Outline each blood parasite and name the species.
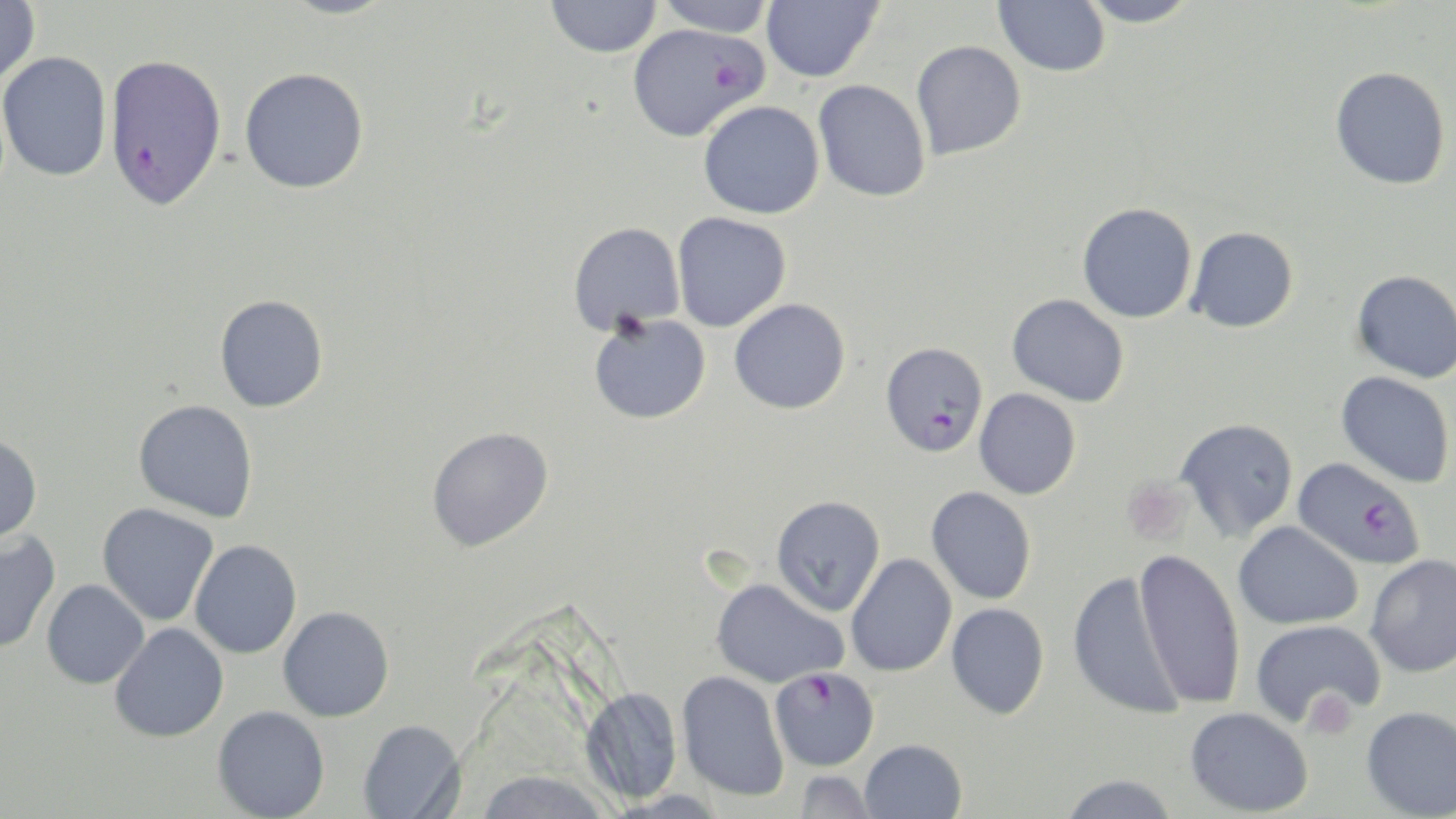
Approximate bounding boxes as (x1, y1, x2, y2) in pixels.
Plasmodium falciparum-infected red blood cells: (626, 22, 766, 142), (104, 53, 227, 209), (881, 341, 989, 457), (1293, 457, 1424, 569), (769, 666, 880, 771).
No Plasmodium ovale, Plasmodium malariae, Plasmodium vivax, Babesia divergens, or Trypanosoma brucei observed.

Platelet locations: (1121, 478, 1193, 544), (1302, 688, 1359, 739). Uninfected red blood cell locations: (0, 0, 41, 88), (275, 0, 401, 19), (545, 0, 662, 57), (654, 0, 776, 37), (761, 0, 883, 82), (1077, 0, 1200, 27), (993, 1, 1112, 75), (910, 40, 1026, 160), (0, 52, 112, 182), (1330, 66, 1451, 190), (239, 67, 369, 193), (813, 79, 931, 202), (698, 100, 825, 219), (1077, 202, 1197, 323), (672, 212, 791, 332), (568, 221, 685, 334), (1187, 226, 1298, 333), (1351, 269, 1456, 383), (214, 294, 329, 412), (1006, 294, 1129, 407), (729, 298, 851, 414), (588, 313, 711, 424), (1336, 371, 1454, 488), (974, 388, 1081, 499), (133, 399, 258, 523), (1176, 418, 1298, 540), (426, 426, 554, 551), (0, 433, 43, 547), (926, 486, 1037, 605), (771, 495, 885, 616), (96, 503, 218, 626), (1233, 521, 1363, 630), (0, 531, 61, 654), (189, 539, 302, 659), (1134, 549, 1246, 710), (846, 553, 957, 677), (1364, 554, 1456, 679), (1068, 570, 1182, 720), (711, 577, 848, 688), (41, 579, 149, 689), (945, 603, 1049, 719), (277, 606, 394, 722), (1250, 619, 1386, 727), (109, 622, 229, 742), (676, 670, 790, 802), (581, 686, 682, 804), (212, 705, 330, 818), (1361, 705, 1456, 818), (1185, 707, 1313, 816), (357, 719, 465, 819), (858, 739, 967, 819), (475, 770, 611, 819), (794, 770, 878, 818), (1058, 774, 1180, 819). Slide-level diagnosis: Plasmodium falciparum. Light microscopy. 1000x magnification. Image is 1456×819 pixels. Thin blood film. May-Grünwald-Giemsa-stained preparation. Single field of view.